Name the blood parasite species.
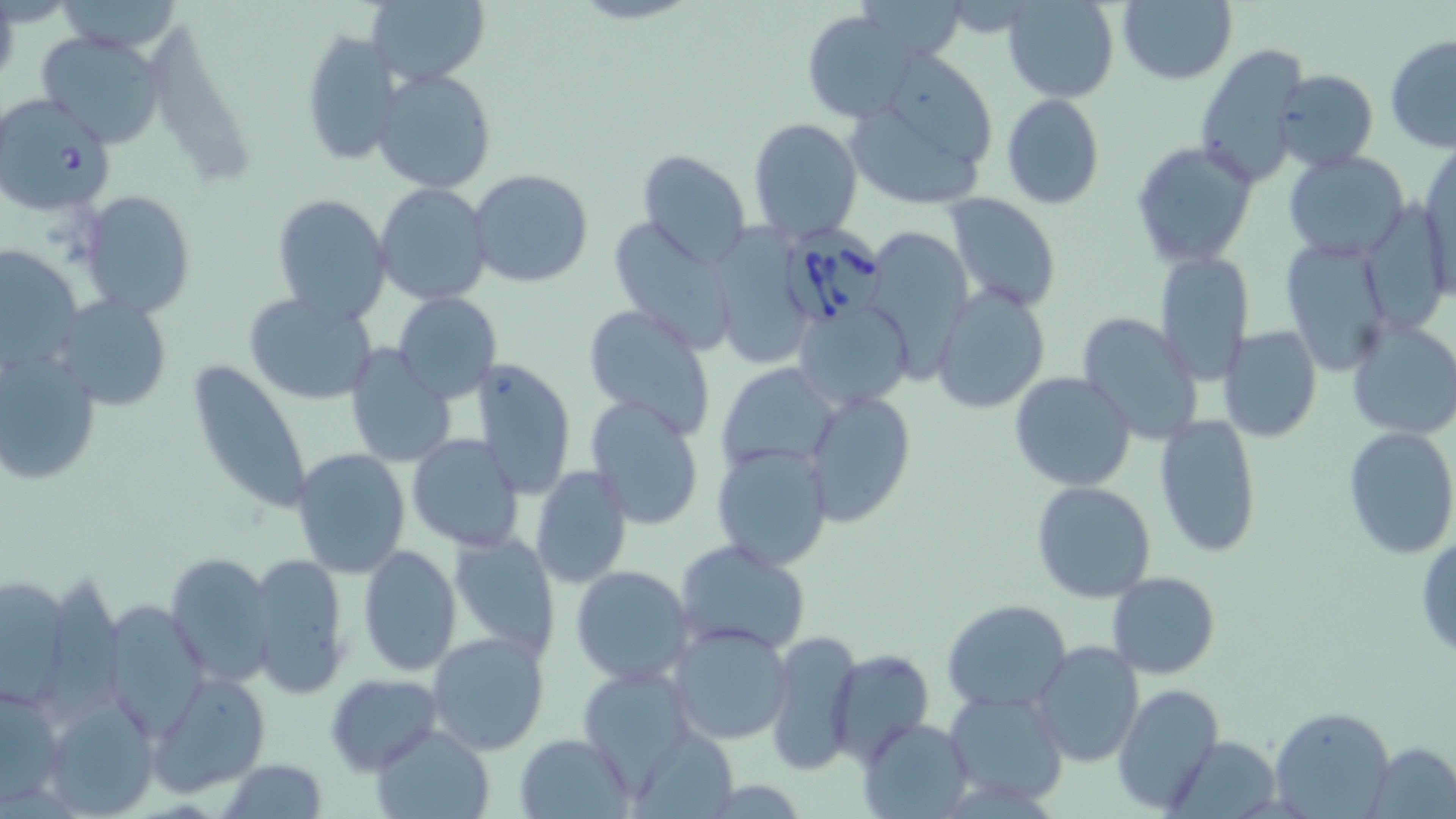

Babesia divergens.

Summary:
  - Coordinate format: approximate bounding boxes as (x1,y1)-(x2,y2) corner pairs in pixels
  - Babesia divergens-infected red blood cell locations: (0,95)-(116,215), (778,223)-(887,332)
  - Uninfected red blood cell locations: (54,0)-(185,55), (365,0)-(490,88), (1004,0)-(1120,103), (1116,0)-(1236,85), (0,1)-(19,87), (804,10)-(918,121), (36,30)-(167,148), (299,30)-(401,166), (1385,34)-(1456,152), (1194,44)-(1310,182), (373,69)-(496,194), (1273,69)-(1379,172), (846,74)-(997,211), (1001,92)-(1106,211), (749,117)-(862,244), (1129,140)-(1258,267), (1421,141)-(1455,286), (1282,149)-(1411,259), (638,150)-(751,268), (468,168)-(593,288), (372,183)-(492,306), (77,190)-(194,317), (944,192)-(1060,312), (271,193)-(392,325), (1371,207)-(1444,339), (612,215)-(729,344), (717,218)-(808,364), (870,228)-(973,382), (1281,239)-(1394,374), (0,246)-(83,374), (1154,249)-(1256,381), (931,286)-(1051,415), (393,291)-(501,403), (243,292)-(377,407), (58,294)-(172,408), (795,300)-(912,408), (582,302)-(715,437), (1076,312)-(1203,444), (1345,315)-(1456,440), (1218,326)-(1321,443), (0,343)-(102,487), (343,345)-(456,468), (185,358)-(313,518), (470,359)-(577,499), (718,363)-(841,476), (1010,372)-(1137,492), (804,389)-(916,526), (585,397)-(706,529), (1154,414)-(1261,558), (1342,426)-(1456,559), (407,434)-(524,553), (293,443)-(531,561), (713,444)-(834,568), (291,450)-(411,578), (529,466)-(632,589), (1030,481)-(1157,603), (448,531)-(560,659), (1416,534)-(1456,662), (675,539)-(812,659), (357,546)-(460,678), (167,553)-(276,686), (247,553)-(350,698), (570,565)-(695,684), (1105,571)-(1219,678), (2,572)-(75,711), (943,599)-(1071,713), (103,603)-(209,739), (668,623)-(794,745), (427,630)-(549,754), (765,630)-(862,772), (1030,641)-(1144,768), (829,650)-(934,762), (148,672)-(272,796), (325,673)-(443,774), (0,679)-(67,810), (1114,682)-(1222,813), (944,688)-(1070,807), (39,692)-(160,818), (1270,706)-(1394,816), (860,717)-(972,815), (368,723)-(495,819), (515,734)-(634,819), (1174,734)-(1284,814), (1370,742)-(1456,817), (220,758)-(326,819)
  - Magnification: 1000x
  - Modality: optical microscopy
  - Image size: 1456×819 pixels
  - Field of view: one of a larger specimen
  - Stain: May-Grünwald-Giemsa
  - Preparation: thin blood smear